Classify the preparation.
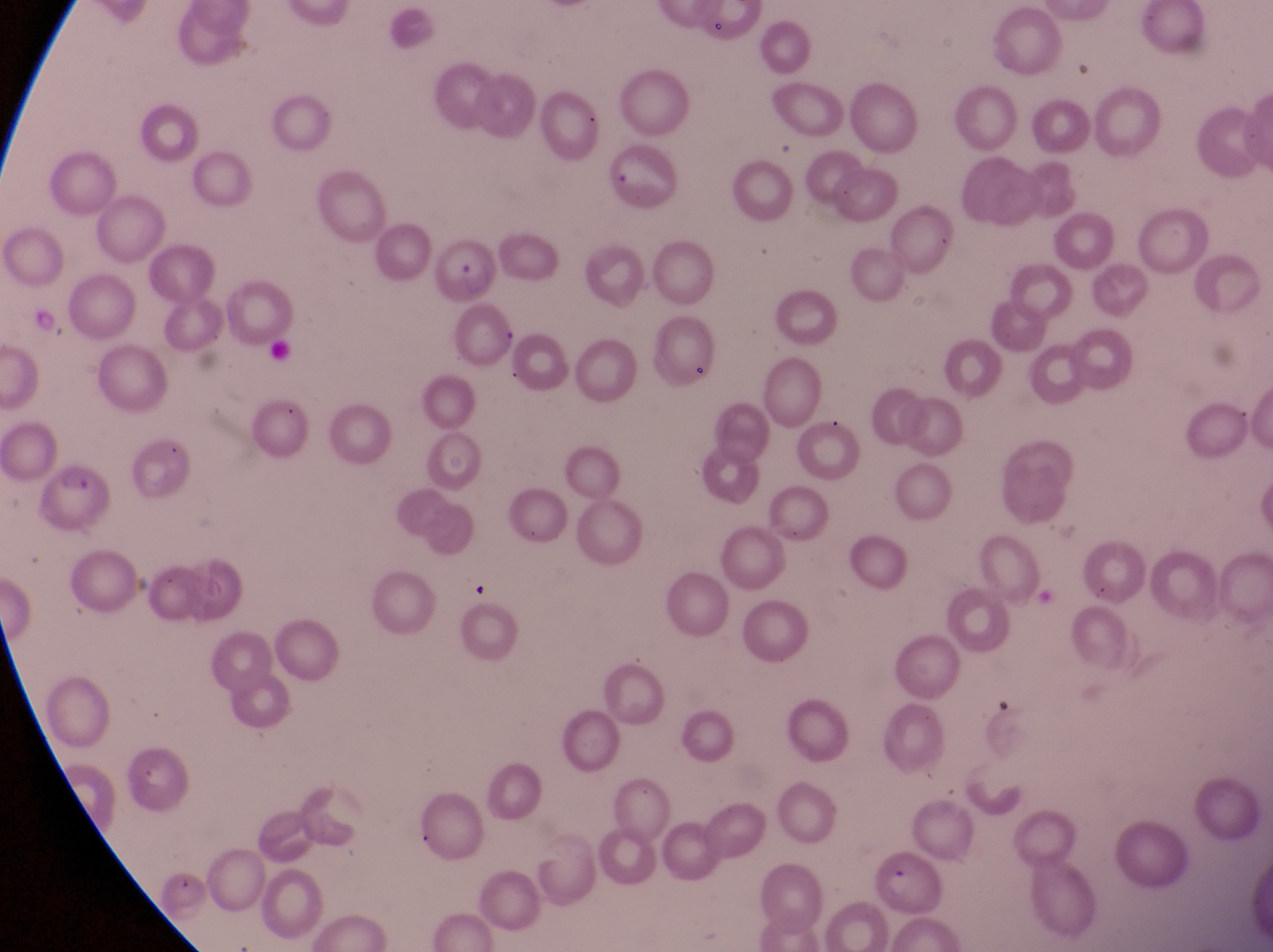

Thin blood smear.

{
  "field_of_view": "single",
  "magnification": "1000x",
  "parasitised_red_blood_cell_locations": "approximate bounding boxes as {left, top, right, bottom} in pixels: {434, 240, 503, 308}, {43, 460, 121, 537}, {880, 840, 942, 913}",
  "country": "Uganda",
  "capture": "smartphone photograph through the eyepiece of an Olympus CX-23 microscope",
  "image_size": "1273×952 pixels"
}